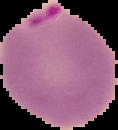 From a thin blood film. Malaria status: parasitized. Image is 118×130 pixels. Segmented cell region on a black background.